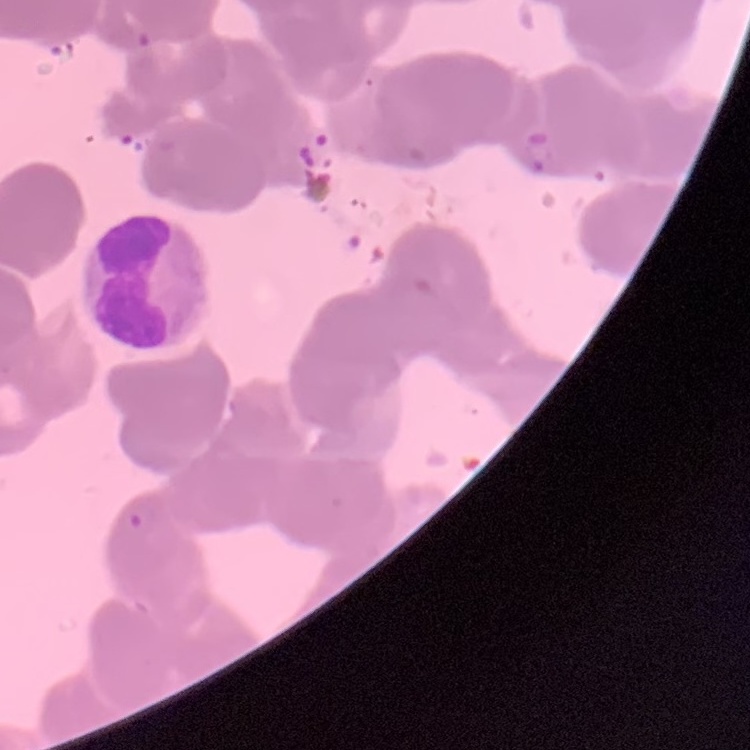
The erythrocytes exhibit rouleaux formation. One tile cut from a larger photomicrograph. Stained with either Field's or Giemsa. Thin blood smear.